Give the position of every Plasmodium parasite visible.
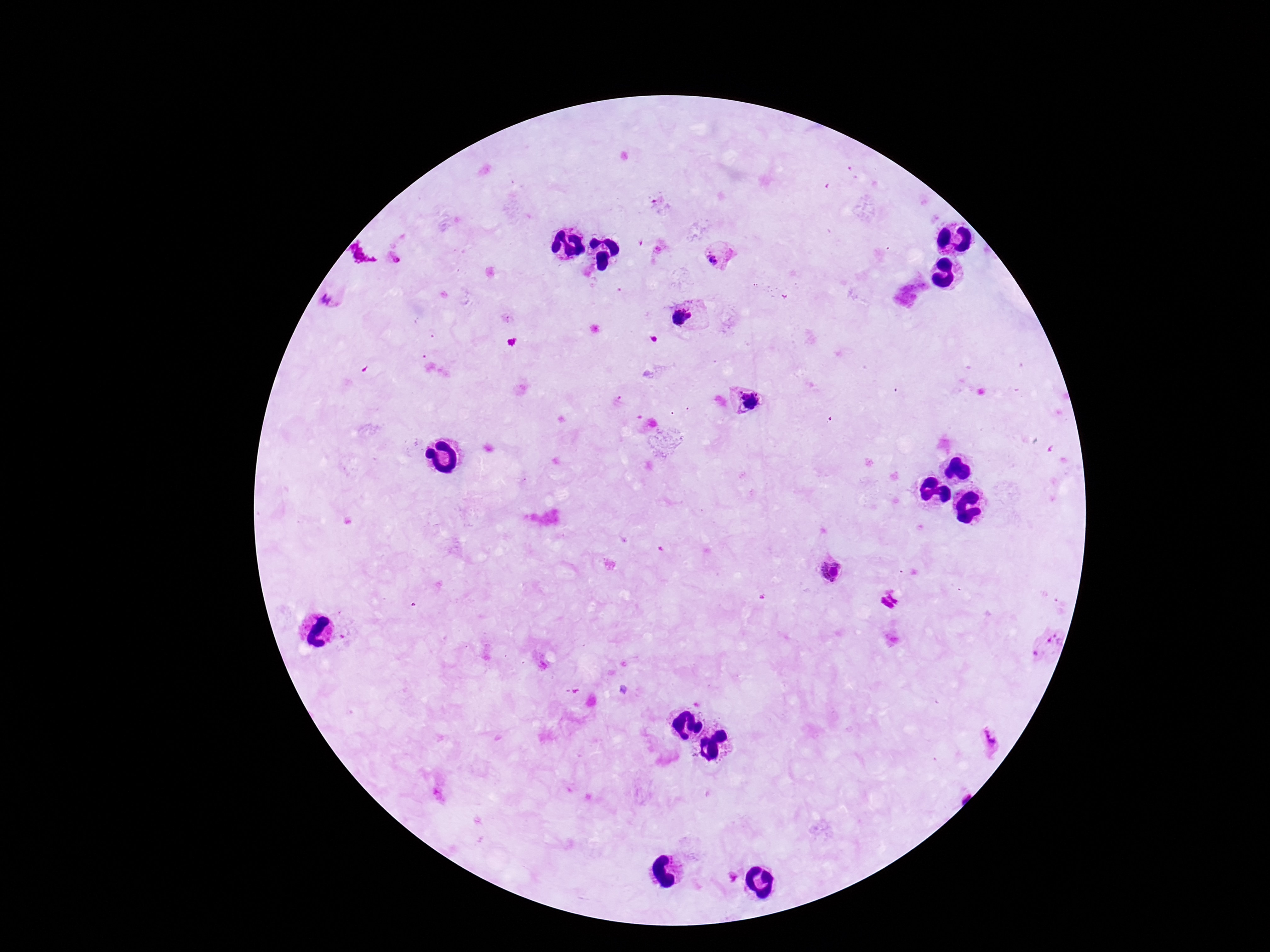
Approximate centers as {x, y} in pixels.
Plasmodium parasites: {655, 200}, {658, 249}, {395, 258}, {716, 259}, {326, 299}, {682, 318}, {743, 394}, {752, 395}, {756, 395}, {751, 405}, {831, 569}, {1057, 637}, {1034, 654}, {989, 739}, {733, 878}.

field of view = single
patient malaria status = positive
image size = 1270×952 pixels
capture = smartphone camera through the microscope eyepiece
preparation = thick blood film
magnification = 100x
stain = Giemsa